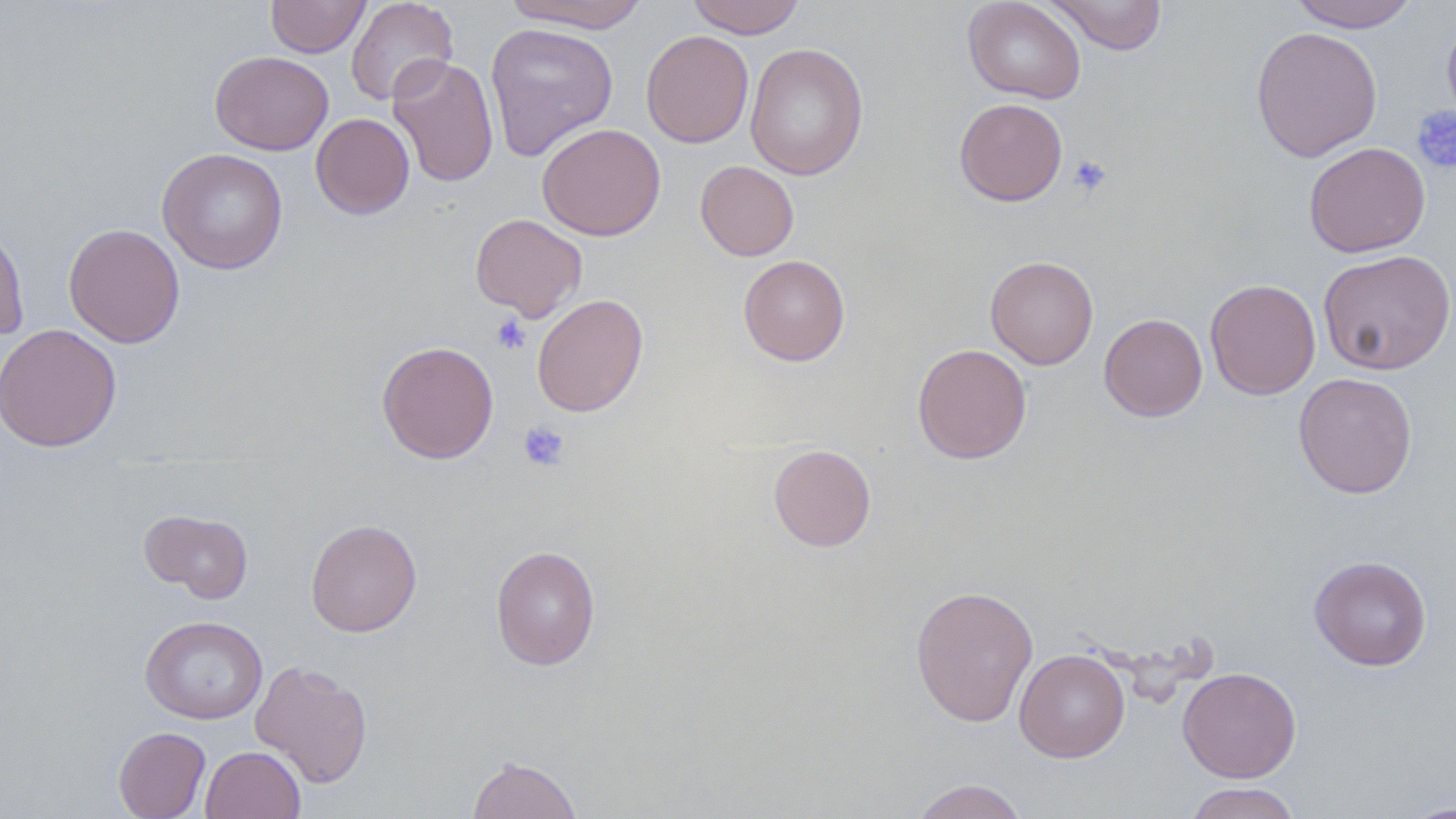

Summary:
  - Coordinate format: approximate bounding boxes as named x1/y1/x2/y2 corners in pixels
  - Uninfected red blood cell locations: (x1=266, y1=0, x2=370, y2=58), (x1=345, y1=0, x2=459, y2=106), (x1=502, y1=0, x2=652, y2=33), (x1=686, y1=0, x2=805, y2=38), (x1=962, y1=0, x2=1086, y2=104), (x1=1046, y1=0, x2=1168, y2=55), (x1=1286, y1=0, x2=1418, y2=31), (x1=1442, y1=16, x2=1456, y2=132), (x1=484, y1=22, x2=619, y2=161), (x1=1250, y1=25, x2=1383, y2=163), (x1=641, y1=30, x2=754, y2=148), (x1=745, y1=42, x2=869, y2=180), (x1=210, y1=51, x2=334, y2=156), (x1=387, y1=54, x2=500, y2=188), (x1=954, y1=97, x2=1068, y2=206), (x1=311, y1=112, x2=415, y2=219), (x1=537, y1=122, x2=666, y2=241), (x1=1303, y1=141, x2=1431, y2=258), (x1=157, y1=147, x2=288, y2=275), (x1=695, y1=160, x2=799, y2=260), (x1=469, y1=213, x2=587, y2=321), (x1=63, y1=223, x2=185, y2=348), (x1=0, y1=224, x2=30, y2=341), (x1=1318, y1=249, x2=1456, y2=376), (x1=738, y1=254, x2=850, y2=366), (x1=985, y1=255, x2=1099, y2=370), (x1=1205, y1=278, x2=1321, y2=400), (x1=532, y1=294, x2=649, y2=417), (x1=1099, y1=313, x2=1207, y2=421), (x1=0, y1=323, x2=122, y2=452), (x1=376, y1=340, x2=499, y2=463), (x1=913, y1=343, x2=1032, y2=464), (x1=1293, y1=372, x2=1417, y2=499), (x1=768, y1=443, x2=876, y2=551), (x1=140, y1=509, x2=254, y2=603), (x1=305, y1=519, x2=422, y2=637), (x1=490, y1=545, x2=601, y2=670), (x1=1309, y1=555, x2=1432, y2=671), (x1=910, y1=584, x2=1039, y2=727), (x1=140, y1=615, x2=268, y2=724), (x1=1014, y1=648, x2=1130, y2=763), (x1=250, y1=659, x2=373, y2=788), (x1=1177, y1=667, x2=1301, y2=782), (x1=113, y1=726, x2=211, y2=819), (x1=201, y1=745, x2=305, y2=818), (x1=467, y1=756, x2=583, y2=819), (x1=910, y1=778, x2=1029, y2=819), (x1=1183, y1=782, x2=1302, y2=819), (x1=1403, y1=802, x2=1456, y2=819)
  - Platelet locations: (x1=1411, y1=106, x2=1456, y2=174), (x1=1067, y1=154, x2=1112, y2=196), (x1=491, y1=314, x2=530, y2=355), (x1=518, y1=421, x2=571, y2=471)
  - Slide-level diagnosis: negative for blood parasites
  - Field of view: single
  - Magnification: 1000x
  - Modality: light microscopy
  - Image size: 1456×819 pixels
  - Stain: May-Grünwald-Giemsa
  - Preparation: thin blood smear